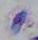

Summary:
  - Magnification: 1000x
  - Modality: photomicrograph
  - Identification: Toxoplasma gondii